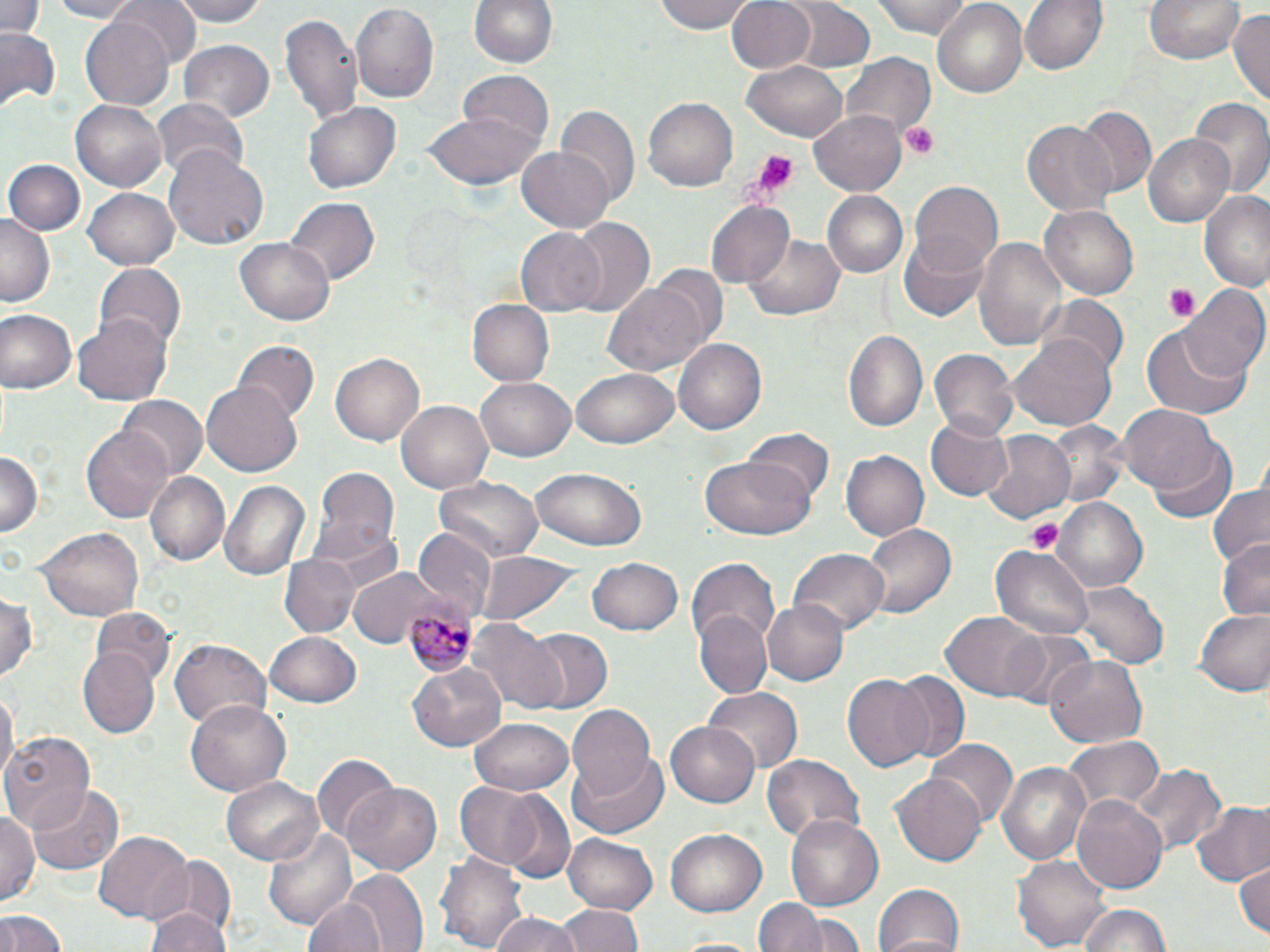

Summary:
  - Coordinate format: approximate bounding boxes as [x1, y1, x2, y2] in pixels
  - Uninfected red blood cell locations: [0, 0, 47, 40], [47, 0, 143, 21], [108, 0, 200, 72], [163, 0, 271, 26], [470, 0, 559, 73], [651, 0, 756, 35], [726, 0, 817, 75], [872, 0, 981, 38], [931, 0, 1029, 98], [1021, 0, 1106, 76], [1145, 0, 1242, 64], [784, 1, 876, 74], [349, 3, 438, 103], [1229, 9, 1270, 106], [281, 11, 363, 129], [81, 16, 175, 107], [0, 25, 62, 111], [179, 41, 273, 123], [844, 56, 935, 136], [744, 61, 850, 143], [458, 72, 554, 148], [642, 94, 738, 190], [70, 97, 167, 190], [1190, 97, 1269, 200], [149, 98, 251, 181], [303, 101, 402, 194], [1076, 106, 1155, 194], [421, 107, 542, 190], [556, 107, 639, 208], [808, 108, 911, 197], [1024, 120, 1118, 215], [1145, 134, 1238, 228], [164, 147, 268, 249], [514, 147, 614, 234], [3, 160, 85, 238], [909, 180, 1004, 277], [85, 188, 180, 270], [820, 191, 909, 278], [1200, 193, 1270, 290], [287, 197, 379, 285], [706, 201, 794, 289], [1040, 204, 1137, 299], [0, 213, 54, 306], [564, 217, 657, 319], [516, 230, 604, 314], [897, 232, 991, 322], [746, 234, 844, 321], [975, 234, 1068, 357], [235, 236, 336, 325], [93, 264, 186, 352], [603, 278, 711, 378], [1183, 283, 1270, 382], [1041, 295, 1128, 378], [468, 300, 555, 387], [1, 310, 77, 393], [73, 311, 173, 407], [1141, 325, 1252, 420], [843, 328, 927, 432], [1009, 338, 1116, 430], [674, 339, 768, 436], [234, 342, 318, 424], [931, 349, 1020, 440], [331, 353, 425, 445], [572, 368, 679, 449], [476, 376, 575, 462], [202, 383, 301, 474], [118, 396, 207, 480], [396, 398, 496, 494], [1119, 404, 1222, 496], [925, 415, 1012, 501], [1042, 420, 1131, 508], [82, 424, 176, 522], [744, 429, 832, 509], [984, 432, 1075, 524], [1149, 440, 1237, 525], [0, 450, 44, 535], [842, 450, 928, 542], [697, 457, 817, 541], [533, 466, 648, 549], [310, 469, 400, 570], [144, 472, 229, 567], [434, 478, 543, 564], [218, 480, 310, 581], [1206, 480, 1269, 568], [1053, 497, 1150, 594], [37, 523, 144, 621], [863, 523, 957, 619], [413, 530, 496, 618], [1216, 538, 1270, 622], [991, 543, 1094, 642], [789, 548, 890, 634], [478, 550, 582, 629], [685, 553, 777, 677], [281, 554, 360, 638], [587, 557, 684, 636], [351, 568, 443, 647], [1074, 579, 1166, 669], [0, 595, 40, 684], [761, 598, 849, 688], [1193, 607, 1270, 696], [91, 608, 174, 686], [693, 609, 775, 701], [942, 611, 1046, 700], [472, 621, 567, 715], [521, 628, 612, 715], [999, 628, 1095, 714], [264, 631, 362, 708], [170, 640, 270, 729], [77, 647, 162, 739], [1045, 655, 1148, 747], [409, 660, 508, 751], [885, 671, 970, 764], [842, 673, 934, 771], [702, 685, 803, 774], [0, 690, 16, 788], [185, 701, 289, 796], [566, 706, 657, 802], [470, 717, 574, 794], [664, 720, 760, 809], [2, 730, 98, 834], [1062, 734, 1166, 820], [928, 740, 1016, 830], [569, 754, 668, 840], [762, 755, 865, 842], [313, 757, 399, 843], [995, 759, 1091, 866], [1132, 765, 1227, 853], [890, 771, 989, 866], [223, 776, 323, 865], [455, 780, 546, 870], [344, 782, 440, 875], [28, 783, 124, 875], [1071, 791, 1167, 895], [500, 792, 574, 881], [1190, 801, 1270, 886], [0, 809, 40, 909], [784, 813, 884, 911], [263, 822, 357, 930], [666, 829, 767, 915], [93, 830, 193, 923], [562, 830, 659, 914], [435, 850, 530, 952], [1012, 853, 1111, 952], [155, 855, 234, 942], [1233, 858, 1270, 938], [338, 869, 430, 952], [874, 883, 967, 952], [302, 895, 386, 952], [756, 895, 824, 951], [1077, 902, 1172, 952], [555, 904, 645, 952], [143, 905, 230, 952], [0, 909, 68, 952], [485, 911, 587, 952], [799, 913, 865, 950], [668, 936, 763, 952]
  - Plasmodium malariae-infected red blood cell locations: [404, 606, 476, 676]
  - Platelet locations: [903, 123, 938, 161], [749, 148, 803, 198], [1161, 283, 1200, 322], [1027, 521, 1063, 556]
  - Slide-level diagnosis: Plasmodium malariae
  - Stain: May-Grünwald-Giemsa
  - Preparation: thin blood smear
  - Modality: optical microscopy
  - Magnification: 1000x
  - Image size: 1270×952 pixels
  - Field of view: single